Report the malaria status of this cell.
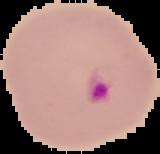

It is parasitized.

image_size: 160×154 pixels
preparation: thin blood film
image_type: segmented cell region on a black background